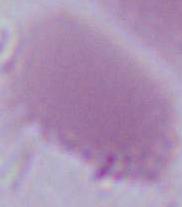
modality = micrograph
magnification = 1000x
identification = red blood cell